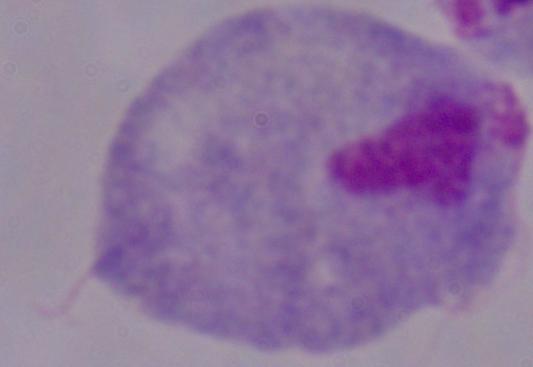
Summary:
  - Magnification: 1000x
  - Identification: trichomonad
  - Modality: micrograph